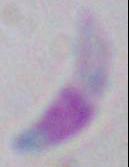
identification = Toxoplasma gondii
modality = micrograph
magnification = 1000x